Outline each Trypanosoma brucei.
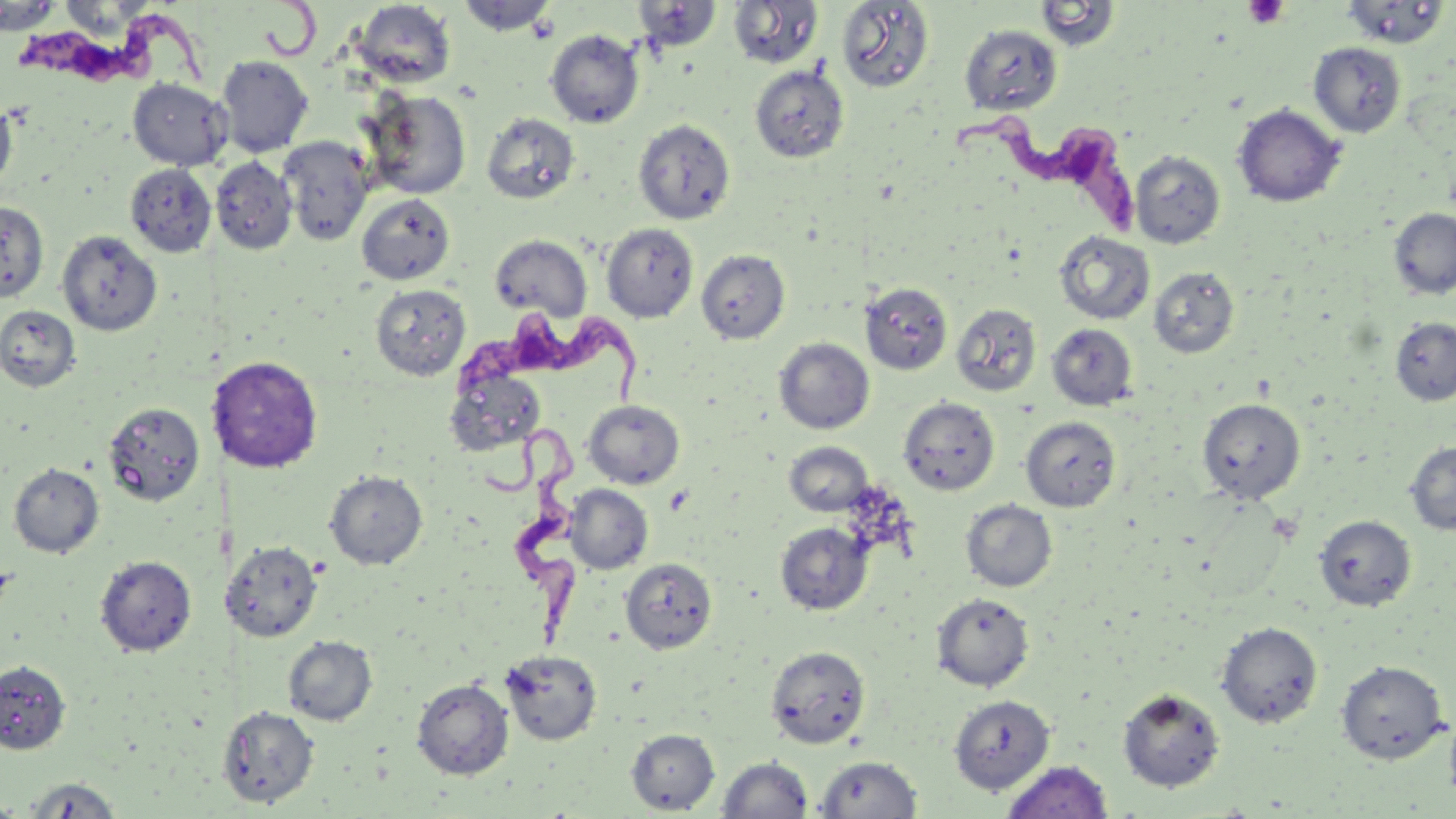
Approximate bounding boxes as (x1,y1)-(x2,y2) corner pairs in pixels.
Trypanosoma brucei: (16,2)-(225,93), (949,113)-(1136,233), (452,302)-(656,406), (491,434)-(584,648).

Uninfected red blood cell locations: (455,0)-(559,36), (727,0)-(823,69), (352,1)-(456,88), (632,1)-(722,53), (835,1)-(935,93), (1034,1)-(1122,51), (1339,1)-(1450,49), (0,3)-(65,35), (959,24)-(1063,115), (545,29)-(644,128), (1309,43)-(1406,138), (216,55)-(314,157), (750,64)-(849,163), (128,78)-(231,170), (362,89)-(471,199), (0,98)-(17,195), (1232,104)-(1346,207), (481,113)-(580,204), (633,119)-(736,224), (278,137)-(373,245), (1130,150)-(1225,249), (210,156)-(297,255), (125,163)-(217,257), (356,194)-(454,285), (0,202)-(49,302), (1389,208)-(1456,299), (601,223)-(698,322), (57,230)-(161,336), (1054,231)-(1155,325), (490,234)-(592,322), (696,249)-(790,344), (1148,266)-(1240,358), (370,283)-(470,381), (861,283)-(952,375), (951,303)-(1042,397), (0,305)-(81,392), (1390,317)-(1456,405), (1046,323)-(1138,410), (774,337)-(874,434), (207,355)-(324,472), (446,363)-(548,456), (899,397)-(999,496), (1197,398)-(1306,504), (102,400)-(206,507), (583,400)-(685,489), (1020,416)-(1120,511), (784,441)-(873,516), (1405,441)-(1456,535), (8,462)-(104,558), (324,470)-(428,570), (565,484)-(653,574), (961,499)-(1058,593), (1315,514)-(1417,611), (774,522)-(873,616), (225,541)-(322,642), (95,555)-(197,656), (620,558)-(717,654), (932,592)-(1034,691), (1216,621)-(1323,728), (283,635)-(378,725), (766,646)-(871,749), (500,649)-(602,746), (0,659)-(71,755), (1336,660)-(1449,763), (412,678)-(513,779), (1117,687)-(1226,793), (949,694)-(1055,793), (217,705)-(319,808), (1444,708)-(1456,807), (626,728)-(719,813), (815,755)-(923,818), (716,757)-(814,818), (1001,760)-(1115,819), (21,776)-(124,818), (1,798)-(23,818). Platelet locations: (1243,0)-(1289,29). Slide-level diagnosis: Trypanosoma brucei. Light microscopy. May-Grünwald-Giemsa-stained preparation. Image is 1456×819 pixels. Single field of view. Thin blood film. Captured at 1000x magnification.